Identify the parasite.
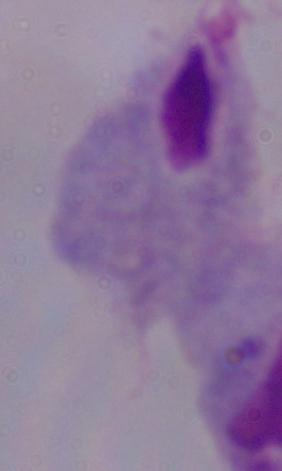
A trichomonad.

Summary:
  - Magnification: 1000x
  - Modality: photomicrograph